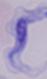
identification = trypanosome
modality = photomicrograph
magnification = 1000x